Assess this cell for malaria.
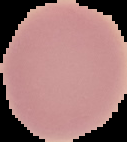

Uninfected.

Segmented cell region on a black background. Image is 127×142 pixels. From a thin blood film.